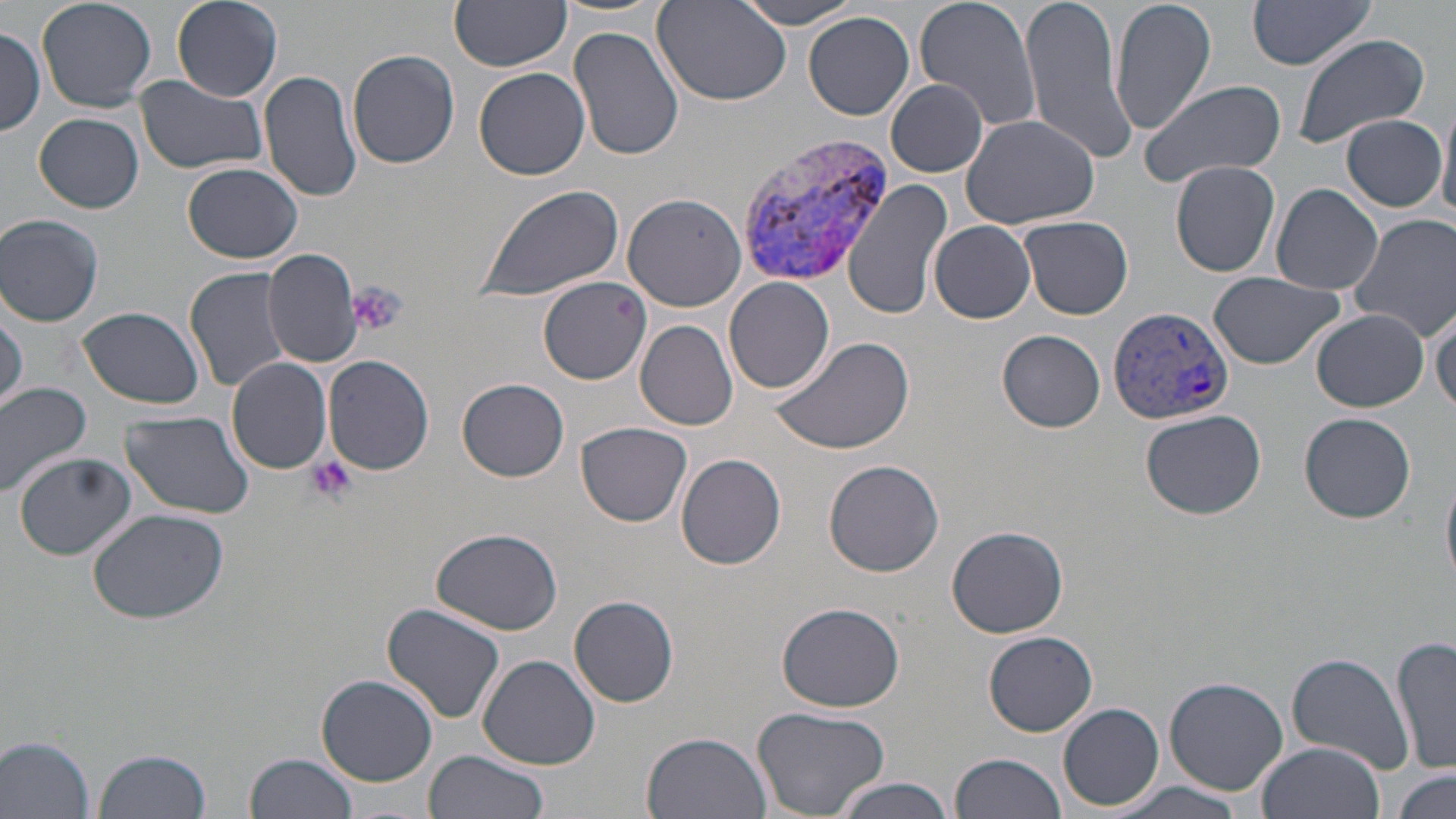
Summary:
  - Coordinate format: approximate bounding boxes as (x1, y1, x2, y2) in pixels
  - Platelet locations: (349, 282, 406, 336), (306, 456, 356, 503)
  - Uninfected red blood cell locations: (38, 0, 158, 113), (171, 0, 282, 102), (649, 0, 794, 107), (728, 0, 867, 28), (914, 0, 1044, 137), (1020, 0, 1134, 163), (1109, 0, 1217, 137), (1248, 0, 1380, 69), (450, 1, 572, 71), (804, 12, 915, 121), (570, 25, 687, 163), (0, 26, 46, 137), (1291, 33, 1432, 150), (347, 49, 461, 170), (475, 66, 591, 180), (260, 68, 363, 204), (135, 75, 267, 175), (886, 79, 989, 178), (1135, 79, 1284, 190), (1438, 101, 1456, 222), (35, 112, 144, 213), (959, 113, 1101, 231), (1341, 115, 1448, 210), (1170, 160, 1281, 276), (183, 164, 306, 265), (844, 176, 951, 318), (1271, 182, 1384, 294), (473, 183, 623, 304), (623, 193, 747, 312), (1, 213, 105, 327), (1348, 214, 1456, 341), (1019, 215, 1133, 319), (928, 220, 1037, 323), (262, 249, 365, 368), (184, 266, 292, 393), (1207, 272, 1345, 369), (540, 276, 652, 383), (723, 277, 835, 395), (1428, 295, 1456, 415), (79, 306, 206, 410), (1312, 310, 1428, 411), (0, 312, 24, 413), (636, 319, 737, 430), (999, 330, 1105, 432), (772, 332, 916, 458), (324, 354, 434, 474), (226, 357, 333, 474), (458, 378, 569, 482), (0, 383, 93, 499), (1139, 408, 1267, 519), (121, 411, 257, 521), (1299, 412, 1417, 523), (575, 422, 692, 527), (17, 453, 136, 560), (675, 455, 788, 570), (822, 460, 945, 577), (1441, 468, 1456, 593), (87, 505, 227, 624), (948, 525, 1068, 638), (431, 529, 563, 635), (569, 595, 679, 707), (775, 602, 907, 713), (381, 603, 509, 726), (984, 631, 1097, 736), (1393, 635, 1456, 776), (1286, 653, 1415, 773), (478, 654, 601, 769), (316, 676, 438, 786), (1164, 677, 1288, 795), (1058, 703, 1164, 811), (753, 705, 890, 818), (641, 731, 769, 819), (1, 736, 97, 816), (1255, 742, 1383, 819), (93, 747, 211, 819), (245, 751, 360, 819), (423, 751, 548, 819), (948, 752, 1068, 819), (1391, 769, 1455, 819), (835, 776, 957, 818), (1103, 779, 1255, 819)
  - Plasmodium vivax-infected red blood cell locations: (731, 130, 890, 285), (1106, 304, 1233, 427)
  - Slide-level diagnosis: Plasmodium vivax
  - Image size: 1456×819 pixels
  - Stain: May-Grünwald-Giemsa
  - Modality: optical microscopy
  - Preparation: thin blood smear
  - Field of view: one of a larger specimen
  - Magnification: 1000x